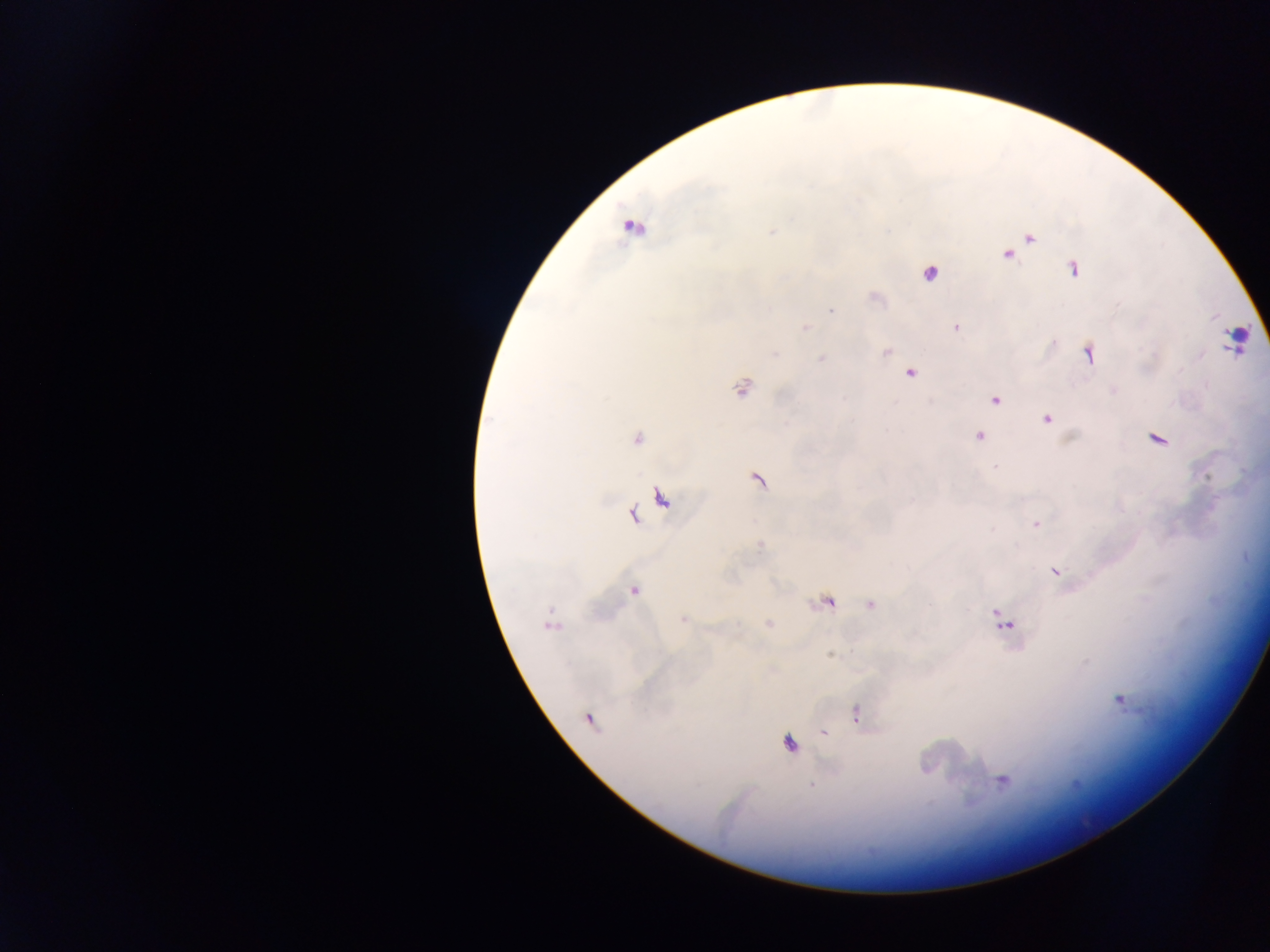
Approximate centers as [x, y] in pixels.
Summary:
  - Leukocyte locations: [1236, 340]
  - Malaria parasite locations: [632, 226], [773, 231], [1029, 238], [1007, 254], [1074, 268], [931, 273], [874, 297], [830, 311], [956, 327], [804, 328], [886, 351], [1089, 353], [821, 359], [909, 372], [742, 387], [1113, 391], [995, 399], [1046, 418], [978, 436], [1157, 438], [636, 439], [758, 480], [661, 498], [633, 514], [1036, 524], [760, 545], [1054, 572], [633, 590], [827, 602], [871, 604], [683, 621], [1003, 621], [768, 623], [550, 624], [830, 655], [1119, 700], [855, 714], [589, 718], [825, 732], [789, 743], [1002, 780], [813, 785]
  - Field of view: single
  - Preparation: thick blood film
  - Country: Ghana
  - Capture: mobile-phone photograph through a microscope
  - Image size: 1270×952 pixels